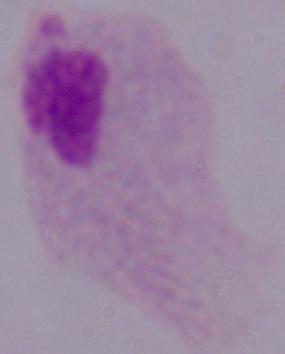
Summary:
  - Identification: trichomonad
  - Magnification: 1000x
  - Modality: micrograph